Locate every malaria parasite and every leukocyte.
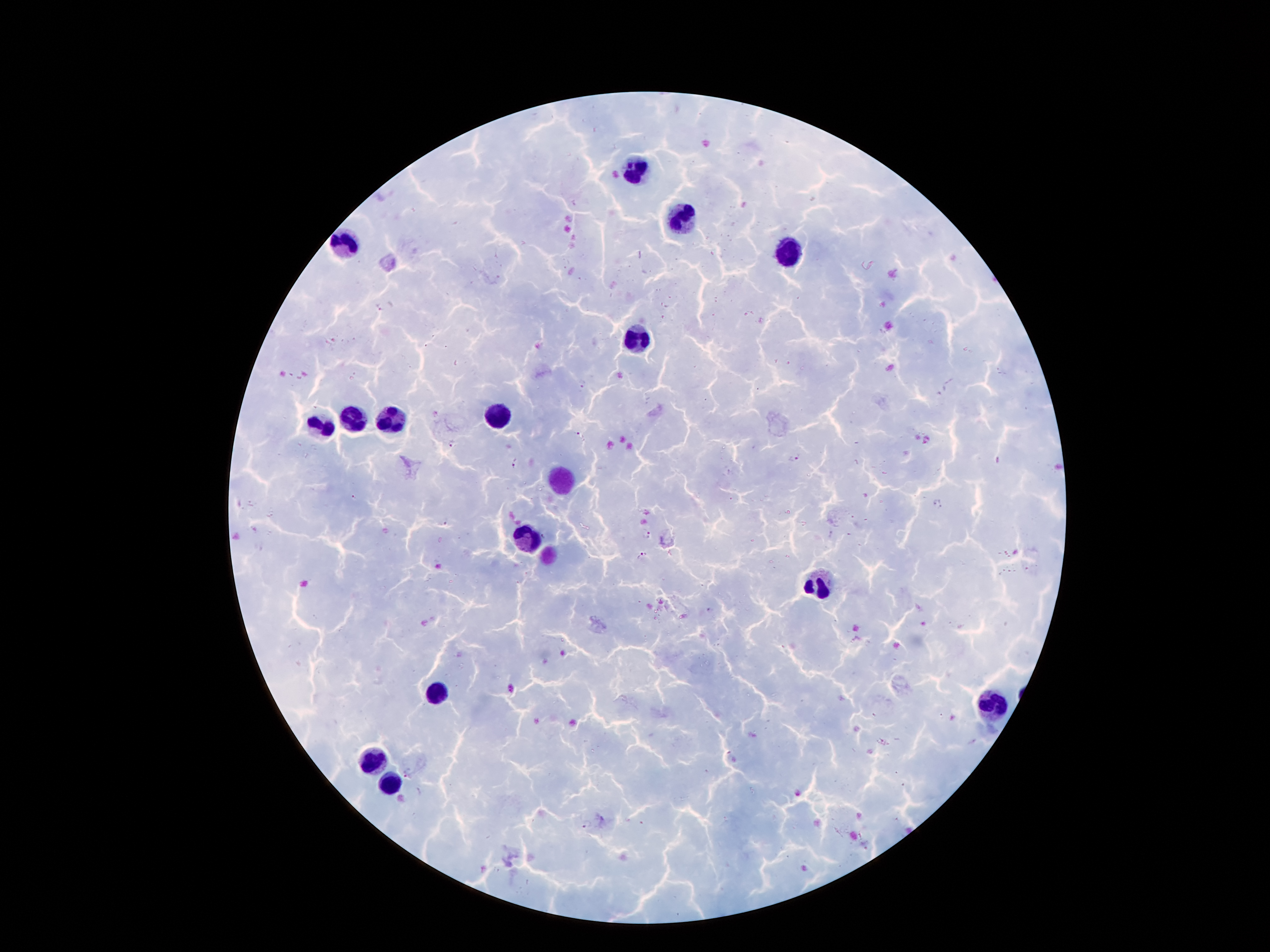

Approximate centers as (x, y) in pixels.
Malaria parasites: (380, 307), (585, 384), (581, 435), (452, 443), (795, 457), (515, 464), (938, 505), (444, 520), (646, 534), (642, 556), (407, 773), (588, 826).
Leukocytes: (634, 169), (683, 219), (347, 246), (785, 250), (639, 341), (354, 416), (500, 416), (393, 418), (321, 427), (528, 535), (814, 584), (442, 692), (993, 708), (374, 761), (387, 785).

Giemsa-stained preparation. Smartphone photograph taken through the microscope eyepiece. 100x magnification. Single field of view. Thick blood film. Patient malaria status: infected with Plasmodium falciparum. Image is 1270×952 pixels.